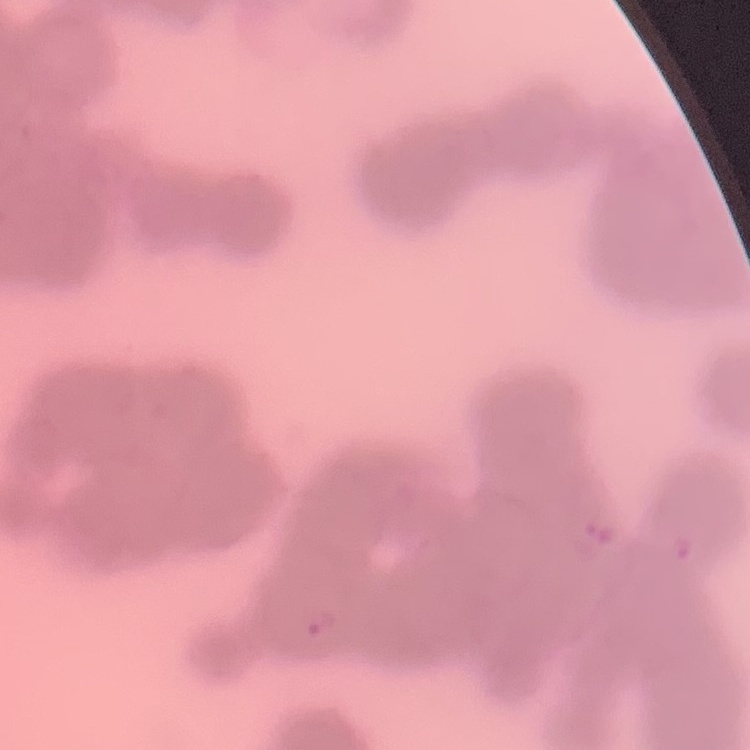
erythrocyte morphology = rouleaux formation
preparation = thin blood film
image type = one tile cut from a larger photomicrograph
stain = Field's or Giemsa